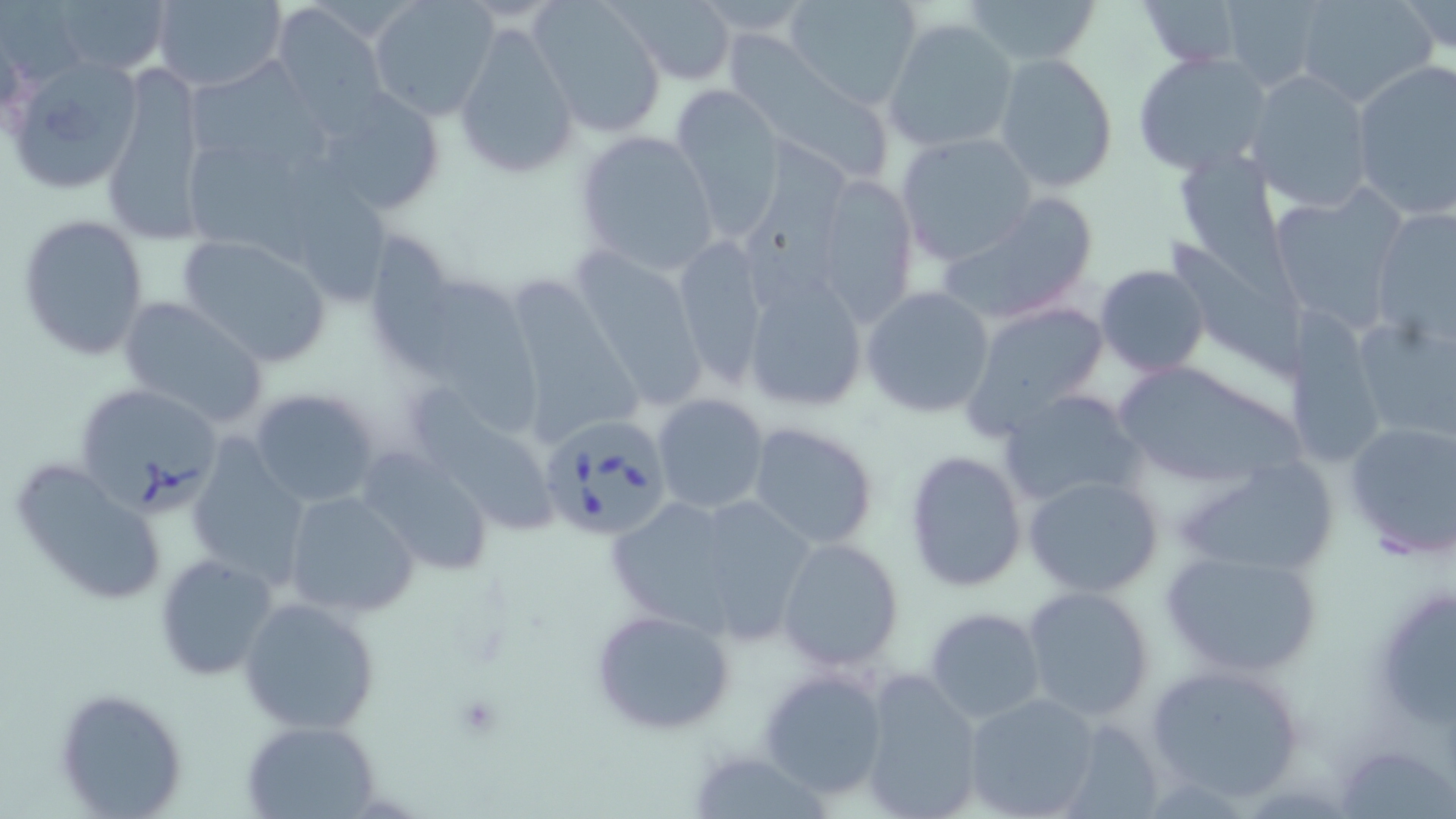
Babesia divergens-infected red blood cell locations = approximate bounding boxes as (x1,y1)-(x2,y2) corner pairs in pixels: (72,383)-(223,514), (537,415)-(671,543)
slide-level diagnosis = Babesia divergens
stain = May-Grünwald-Giemsa
modality = optical microscopy
image size = 1456×819 pixels
magnification = 1000x
preparation = thin blood film
uninfected red blood cell locations = approximate bounding boxes as (x1,y1)-(x2,y2) corner pairs in pixels: (49,0)-(174,78), (153,0)-(286,93), (367,0)-(499,121), (530,0)-(668,136), (785,0)-(922,110), (963,0)-(1101,67), (1294,0)-(1438,108), (1137,1)-(1250,69), (268,2)-(392,125), (614,2)-(737,84), (1394,2)-(1456,61), (1210,3)-(1330,89), (883,17)-(1019,154), (452,18)-(579,180), (727,29)-(900,189), (1133,50)-(1272,176), (992,53)-(1120,195), (184,55)-(327,178), (5,56)-(144,194), (1350,59)-(1456,219), (101,65)-(210,246), (1244,69)-(1375,213), (313,85)-(448,217), (667,88)-(784,234), (573,128)-(719,272), (896,131)-(1038,266), (741,133)-(861,285), (186,145)-(325,277), (1173,145)-(1287,270), (811,174)-(918,324), (269,175)-(396,306), (1268,190)-(1408,326), (940,192)-(1099,325), (1371,209)-(1455,343), (17,214)-(149,362), (375,230)-(459,374), (176,234)-(333,367), (669,236)-(768,387), (1168,236)-(1312,378), (576,247)-(706,408), (1095,264)-(1209,378), (511,272)-(650,441), (741,272)-(868,414), (433,273)-(544,439), (862,286)-(995,418), (116,295)-(271,430), (961,301)-(1111,433), (1351,306)-(1456,441), (1289,312)-(1385,474), (1110,358)-(1306,488), (249,386)-(383,508), (998,387)-(1144,511), (413,391)-(556,546), (653,393)-(771,514), (1342,417)-(1456,559), (747,421)-(880,550), (184,439)-(313,589), (904,449)-(1028,591), (358,450)-(494,577), (9,457)-(168,606), (1172,457)-(1342,581), (1023,474)-(1165,598), (282,490)-(420,620), (707,499)-(815,646), (613,507)-(744,637), (776,537)-(904,671), (1160,544)-(1325,678), (153,553)-(279,683), (1378,584)-(1456,740), (1021,585)-(1155,722), (239,596)-(381,736), (922,607)-(1047,725), (589,608)-(736,736), (1145,662)-(1310,802), (759,668)-(891,802), (857,671)-(983,818), (55,686)-(191,817), (963,691)-(1102,818), (242,720)-(381,818), (1338,746)-(1456,818), (696,752)-(832,819)
platelet locations = approximate bounding boxes as (x1,y1)-(x2,y2) corner pairs in pixels: (451,693)-(503,737)
field of view = single